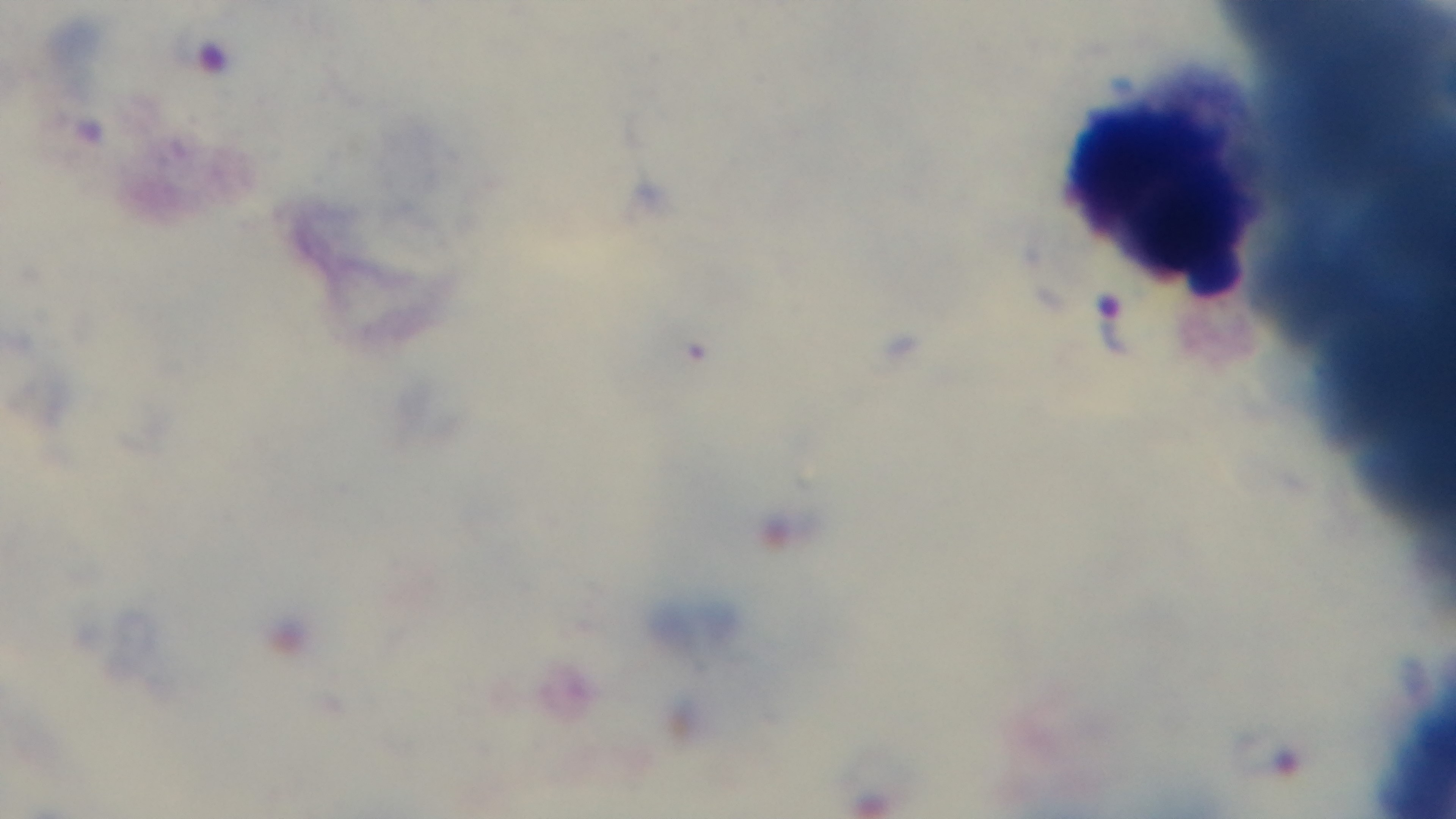
{
  "objective": "100x oil immersion",
  "field_of_view": "one from the slide",
  "stain": "Giemsa",
  "capture": "mounted 4K digital camera",
  "malaria_status": "positive",
  "preparation": "thick blood film",
  "modality": "light microscopy"
}